Report the malaria status of this cell.
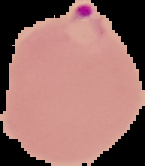

Parasitized.

Summary:
  - Image size: 145×166 pixels
  - Preparation: thin blood film
  - Image type: segmented cell region on a black background